Classify this cell by malaria status.
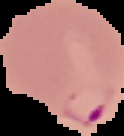

Parasitized.

The area outside the segmented cell region is set to black. From a thin blood smear. Image is 124×136 pixels.